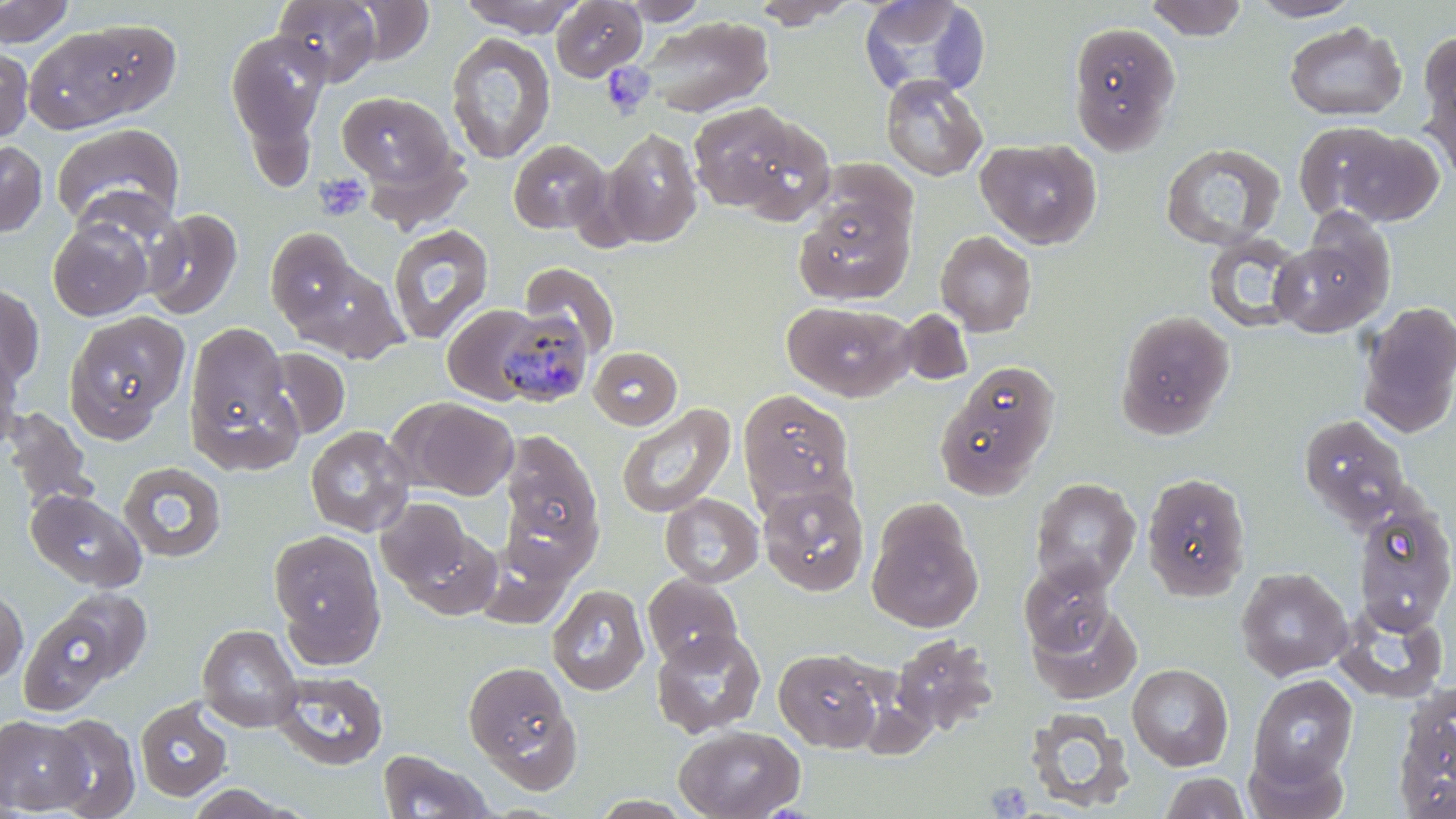

slide-level diagnosis = Plasmodium malariae
image size = 1456×819 pixels
uninfected red blood cell locations = approximate bounding boxes as named x1/y1/x2/y2 corners in pixels: (x1=0, y1=0, x2=75, y2=47), (x1=273, y1=0, x2=381, y2=85), (x1=347, y1=0, x2=435, y2=63), (x1=459, y1=0, x2=586, y2=37), (x1=619, y1=0, x2=709, y2=26), (x1=750, y1=0, x2=860, y2=28), (x1=858, y1=0, x2=988, y2=98), (x1=1145, y1=0, x2=1247, y2=41), (x1=1247, y1=0, x2=1365, y2=22), (x1=551, y1=1, x2=647, y2=81), (x1=639, y1=16, x2=773, y2=118), (x1=62, y1=17, x2=184, y2=119), (x1=1067, y1=21, x2=1182, y2=154), (x1=1283, y1=21, x2=1407, y2=122), (x1=23, y1=26, x2=147, y2=133), (x1=225, y1=29, x2=331, y2=146), (x1=1419, y1=31, x2=1456, y2=131), (x1=446, y1=32, x2=557, y2=164), (x1=0, y1=45, x2=33, y2=143), (x1=1420, y1=63, x2=1456, y2=187), (x1=880, y1=74, x2=988, y2=181), (x1=337, y1=90, x2=457, y2=191), (x1=688, y1=101, x2=833, y2=221), (x1=1292, y1=121, x2=1409, y2=224), (x1=50, y1=122, x2=185, y2=235), (x1=601, y1=126, x2=703, y2=249), (x1=1339, y1=132, x2=1445, y2=228), (x1=976, y1=137, x2=1102, y2=249), (x1=0, y1=139, x2=48, y2=237), (x1=508, y1=139, x2=610, y2=234), (x1=1159, y1=142, x2=1285, y2=251), (x1=810, y1=159, x2=917, y2=245), (x1=795, y1=199, x2=914, y2=304), (x1=143, y1=208, x2=243, y2=320), (x1=47, y1=217, x2=153, y2=321), (x1=387, y1=223, x2=494, y2=344), (x1=263, y1=227, x2=357, y2=329), (x1=1271, y1=229, x2=1391, y2=338), (x1=935, y1=230, x2=1037, y2=337), (x1=1203, y1=234, x2=1308, y2=333), (x1=289, y1=260, x2=408, y2=363), (x1=520, y1=262, x2=620, y2=359), (x1=0, y1=283, x2=45, y2=390), (x1=782, y1=301, x2=914, y2=402), (x1=1357, y1=301, x2=1456, y2=438), (x1=442, y1=305, x2=542, y2=404), (x1=897, y1=309, x2=974, y2=387), (x1=1115, y1=309, x2=1235, y2=440), (x1=63, y1=311, x2=189, y2=441), (x1=184, y1=320, x2=299, y2=465), (x1=0, y1=343, x2=24, y2=455), (x1=265, y1=346, x2=351, y2=440), (x1=589, y1=347, x2=682, y2=429), (x1=934, y1=360, x2=1061, y2=499), (x1=737, y1=388, x2=855, y2=511), (x1=399, y1=398, x2=518, y2=500), (x1=616, y1=402, x2=736, y2=518), (x1=2, y1=407, x2=96, y2=512), (x1=1298, y1=413, x2=1413, y2=528), (x1=305, y1=425, x2=415, y2=537), (x1=499, y1=429, x2=604, y2=564), (x1=118, y1=460, x2=227, y2=562), (x1=1141, y1=471, x2=1252, y2=601), (x1=1030, y1=478, x2=1142, y2=594), (x1=758, y1=483, x2=870, y2=595), (x1=25, y1=489, x2=146, y2=592), (x1=660, y1=493, x2=764, y2=587), (x1=378, y1=497, x2=476, y2=596), (x1=867, y1=501, x2=983, y2=634), (x1=1352, y1=502, x2=1456, y2=635), (x1=269, y1=528, x2=386, y2=660), (x1=1019, y1=559, x2=1117, y2=656), (x1=1235, y1=567, x2=1354, y2=681), (x1=642, y1=574, x2=744, y2=669), (x1=547, y1=584, x2=649, y2=696), (x1=0, y1=587, x2=28, y2=684), (x1=55, y1=588, x2=152, y2=683), (x1=1028, y1=601, x2=1141, y2=704), (x1=1333, y1=601, x2=1449, y2=704), (x1=18, y1=606, x2=121, y2=715), (x1=198, y1=624, x2=302, y2=732), (x1=650, y1=629, x2=766, y2=738), (x1=890, y1=634, x2=998, y2=736), (x1=773, y1=648, x2=883, y2=751), (x1=462, y1=659, x2=580, y2=785), (x1=1127, y1=663, x2=1234, y2=770), (x1=272, y1=670, x2=388, y2=771), (x1=1249, y1=673, x2=1357, y2=785), (x1=1393, y1=682, x2=1456, y2=816), (x1=135, y1=699, x2=232, y2=801), (x1=1024, y1=708, x2=1135, y2=812), (x1=44, y1=713, x2=140, y2=818), (x1=0, y1=715, x2=91, y2=814), (x1=673, y1=724, x2=805, y2=819), (x1=1243, y1=746, x2=1349, y2=819), (x1=378, y1=749, x2=494, y2=818), (x1=1160, y1=771, x2=1250, y2=818), (x1=183, y1=784, x2=300, y2=818)
stain = May-Grünwald-Giemsa
modality = optical microscopy
magnification = 1000x
preparation = thin blood smear
Plasmodium malariae-infected red blood cell locations = approximate bounding boxes as named x1/y1/x2/y2 corners in pixels: (x1=494, y1=308, x2=593, y2=406)
platelet locations = approximate bounding boxes as named x1/y1/x2/y2 corners in pixels: (x1=601, y1=62, x2=655, y2=119), (x1=313, y1=173, x2=370, y2=222), (x1=986, y1=780, x2=1033, y2=817)
field of view = single